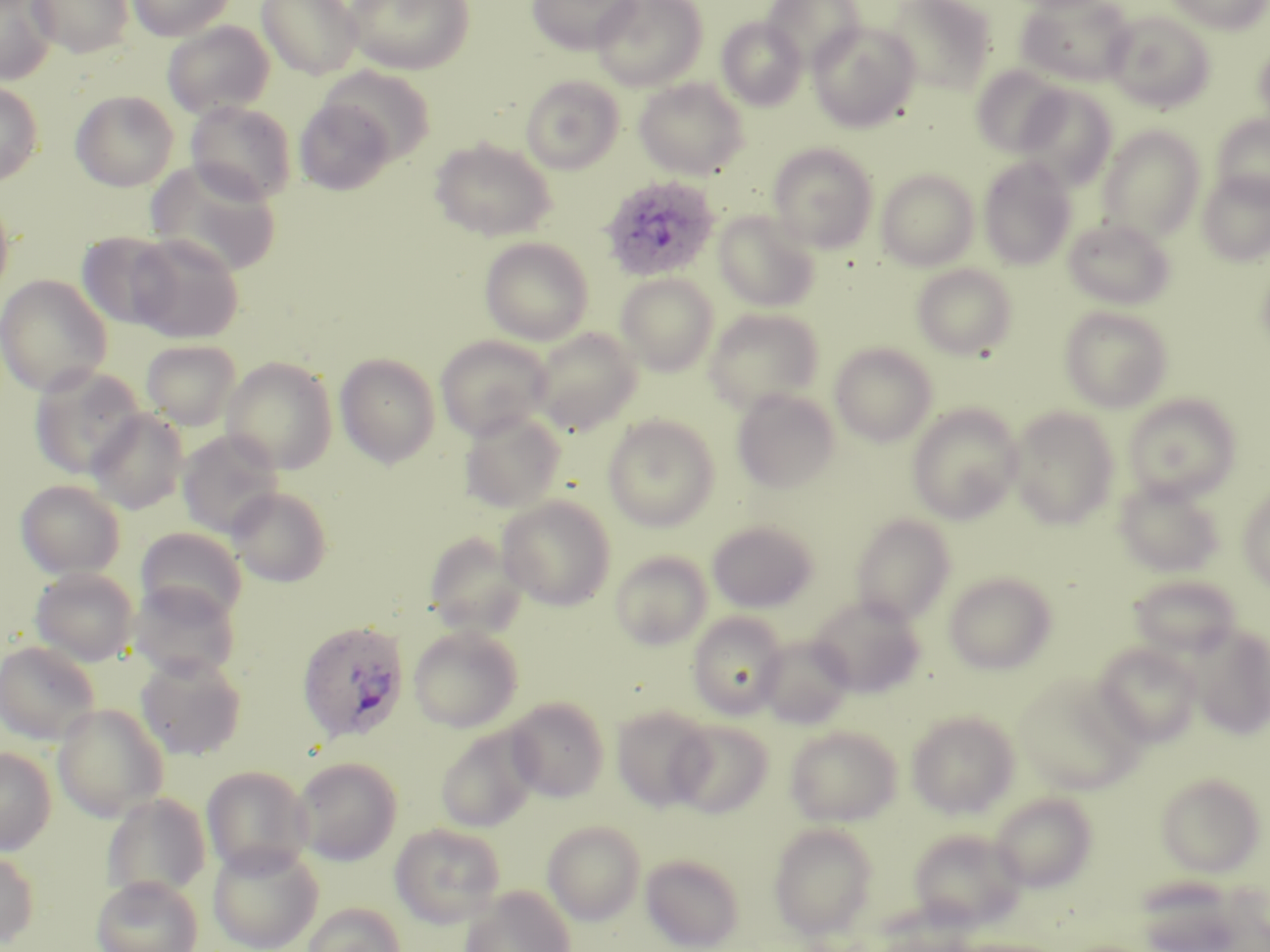
{
  "slide_level_diagnosis": "Plasmodium ovale",
  "stain": "May-Grünwald-Giemsa",
  "plasmodium_ovale_infected_red_blood_cell_locations": "approximate bounding boxes as (x1,y1)-(x2,y2) corner pairs in pixels: (600,175)-(721,282), (296,620)-(411,743)",
  "field_of_view": "one of a larger specimen",
  "modality": "optical microscopy",
  "image_size": "1270×952 pixels",
  "preparation": "thin blood smear",
  "uninfected_red_blood_cell_locations": "approximate bounding boxes as (x1,y1)-(x2,y2) corner pairs in pixels: (0,0)-(57,84), (29,0)-(133,58), (126,0)-(236,41), (257,0)-(363,79), (344,0)-(474,75), (526,0)-(639,54), (591,0)-(707,90), (762,0)-(864,71), (887,0)-(997,94), (1016,0)-(1134,86), (1166,0)-(1268,33), (1103,9)-(1215,113), (716,16)-(807,110), (162,20)-(275,119), (808,20)-(920,132), (1252,39)-(1270,132), (319,66)-(436,165), (971,66)-(1067,157), (520,75)-(625,174), (634,78)-(749,179), (0,81)-(43,186), (1015,85)-(1117,190), (70,90)-(179,192), (294,98)-(396,194), (185,100)-(297,204), (1211,114)-(1270,207), (1098,126)-(1205,241), (429,137)-(557,241), (768,142)-(878,253), (978,156)-(1077,270), (146,160)-(283,278), (876,168)-(979,270), (1198,171)-(1270,266), (0,193)-(14,301), (713,210)-(821,312), (1063,217)-(1176,309), (78,231)-(181,329), (127,233)-(244,343), (480,237)-(594,345), (1256,260)-(1270,358), (911,263)-(1018,360), (615,273)-(719,376), (0,274)-(112,397), (1059,305)-(1174,412), (703,308)-(824,413), (530,327)-(642,434), (435,334)-(553,440), (140,340)-(241,431), (829,342)-(938,446), (335,353)-(440,468), (221,356)-(338,474), (29,364)-(147,479), (732,388)-(840,493), (1123,393)-(1241,502), (907,403)-(1024,525), (1007,406)-(1120,530), (86,408)-(189,514), (458,409)-(566,512), (603,414)-(720,532), (177,430)-(284,539), (1114,476)-(1225,577), (16,479)-(126,579), (1238,485)-(1270,591), (228,486)-(332,587), (496,496)-(616,610), (850,513)-(955,624), (707,520)-(818,613), (136,527)-(247,623), (423,532)-(530,638), (610,550)-(712,650), (30,567)-(138,666), (943,571)-(1057,675), (1128,574)-(1244,659), (128,581)-(241,682), (808,594)-(926,697), (688,612)-(788,719), (408,625)-(523,732), (1189,625)-(1270,740), (757,635)-(854,729), (0,640)-(101,744), (1092,643)-(1201,747), (136,654)-(247,760), (1015,673)-(1146,796), (505,697)-(609,802), (52,704)-(169,821), (611,705)-(715,812), (906,710)-(1020,818), (669,719)-(774,818), (785,725)-(902,826), (435,726)-(540,833), (0,746)-(56,855), (292,757)-(403,866), (201,766)-(313,877), (1155,772)-(1266,877), (989,791)-(1098,893), (101,793)-(211,901), (542,821)-(645,925), (390,823)-(506,927), (768,823)-(877,939), (906,828)-(1027,930), (207,842)-(323,952), (0,850)-(39,949), (640,853)-(745,951), (91,875)-(203,952), (461,885)-(574,952), (302,902)-(406,952)",
  "magnification": "1000x"
}